Assess this cell for malaria.
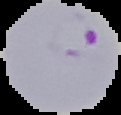

It is parasitized.

image type = segmented cell region with the area outside set to black
preparation = thin blood film
image size = 121×115 pixels